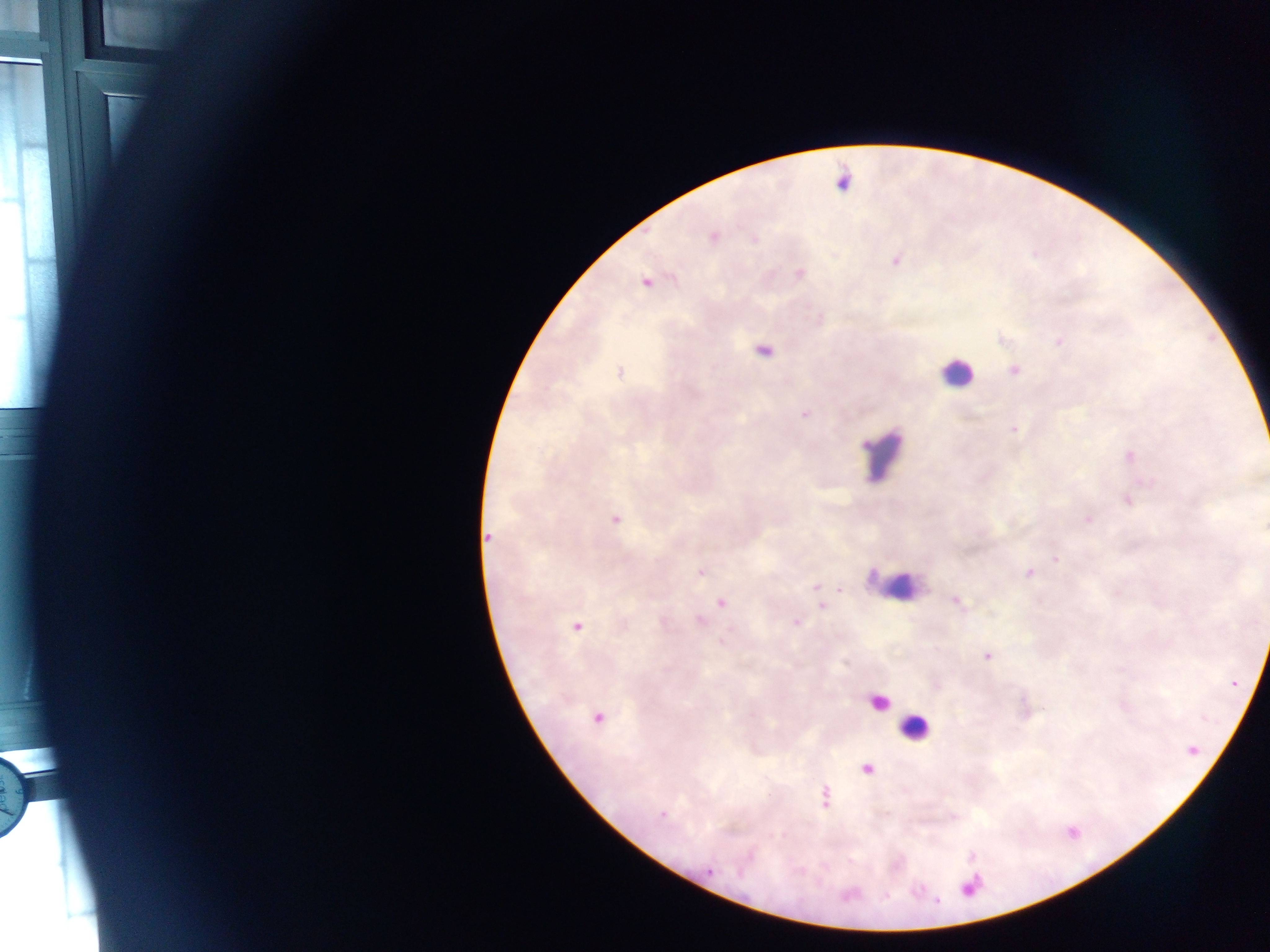
image size = 1270×952 pixels
leukocyte locations = approximate centers as [x, y] in pixels: [956, 373], [883, 453], [892, 582], [879, 702], [914, 727]
country = Ghana
capture = mobile-phone photograph through a microscope
field of view = single
preparation = thick blood smear
malaria parasite locations = approximate centers as [x, y] in pixels: [713, 236], [753, 239], [895, 261], [800, 273], [645, 283], [1059, 341], [764, 351], [1014, 371], [621, 372], [805, 414], [1014, 430], [1130, 455], [1128, 502], [615, 519], [1088, 519], [488, 536], [1056, 559], [700, 572], [1029, 573], [815, 587], [957, 602], [722, 603], [822, 607], [701, 620], [796, 622], [577, 626], [987, 656], [598, 718], [1194, 750], [867, 769], [825, 797], [662, 815], [710, 871], [969, 888], [886, 896], [938, 901]